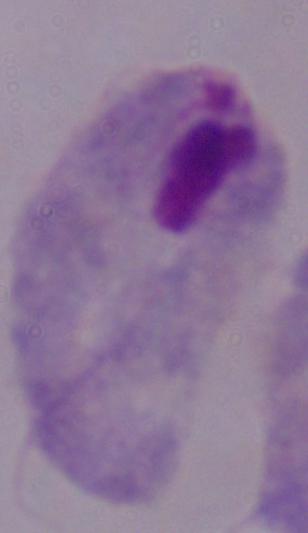
A trichomonad is shown. Captured at 1000x magnification. Micrograph.